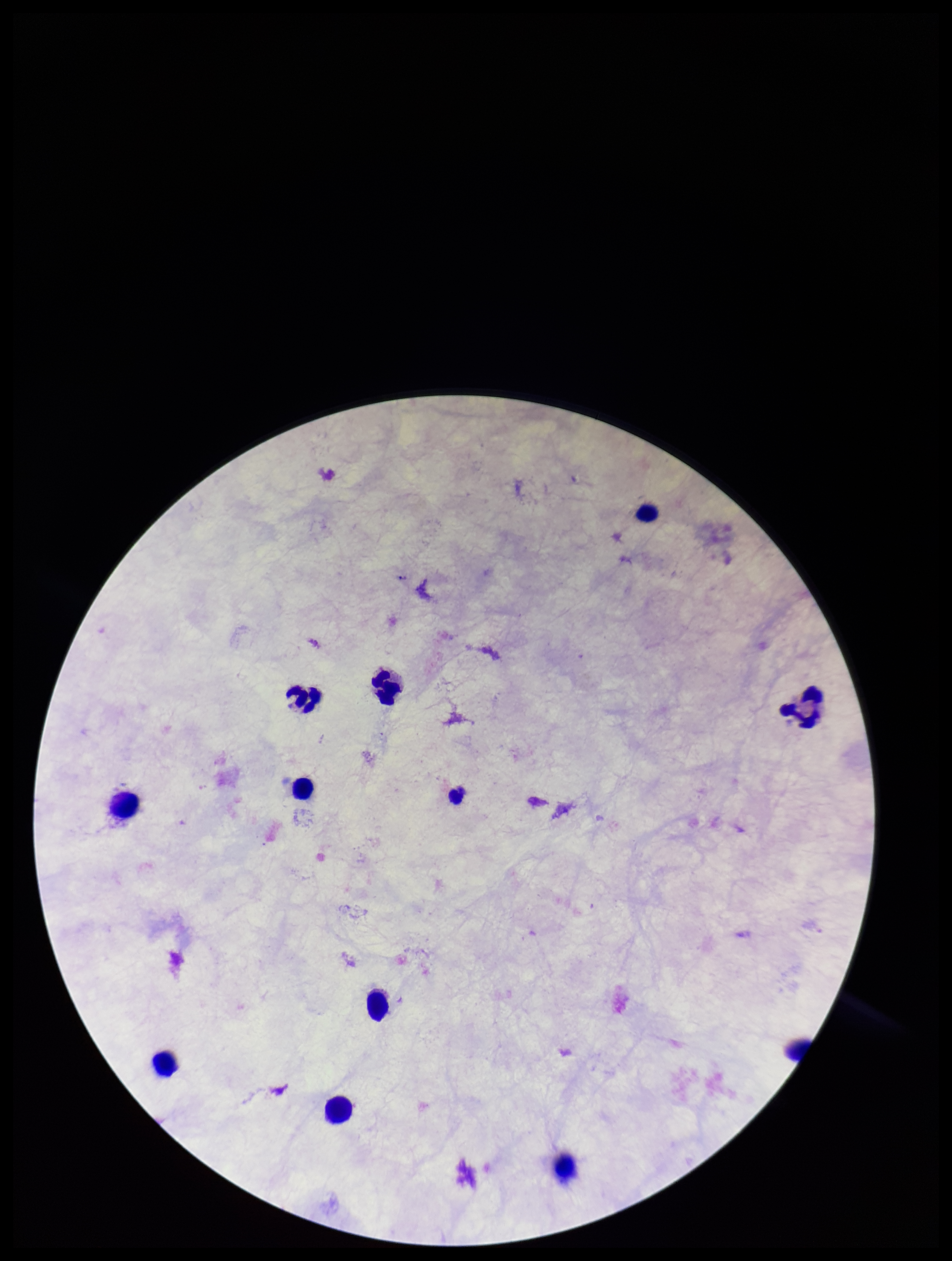

{
  "preparation": "thick smear",
  "stain": "Giemsa",
  "leukocyte_count": 11,
  "capture": "smartphone photograph through the microscope eyepiece",
  "plasmodium_parasites": "none detected",
  "parasite_count": 0,
  "field_of_view": "one from this slide",
  "image_size": "952×1261 pixels",
  "patient_malaria_status": "negative"
}